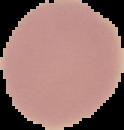

Summary:
  - Malaria status: uninfected
  - Image size: 124×130 pixels
  - Image type: cell region segmented out of the field of view; surrounding area masked to black
  - Preparation: thin blood smear